Identify the parasite.
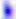

Toxoplasma gondii.

Summary:
  - Magnification: 400x
  - Modality: photomicrograph